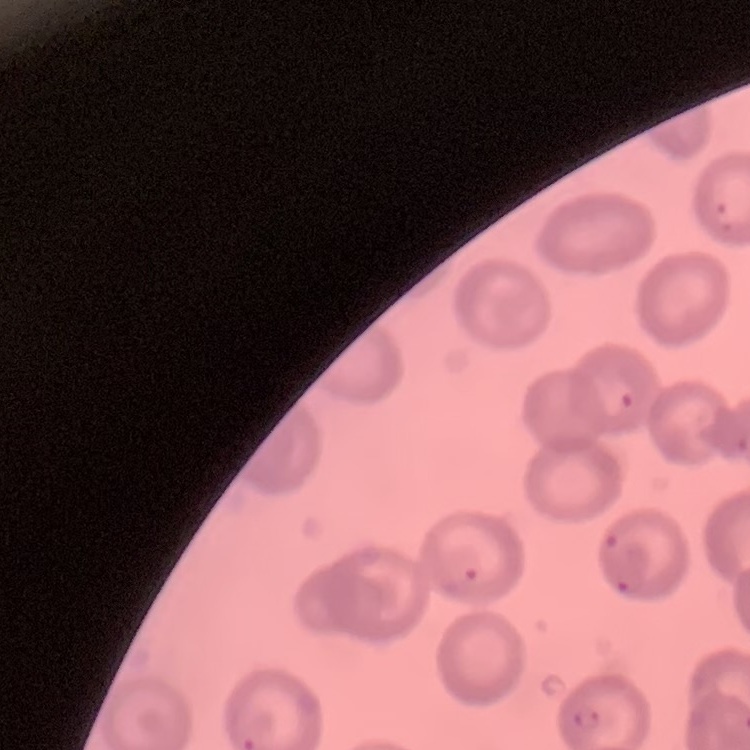
Summary:
  - Erythrocyte morphology: no rouleaux formation
  - Image type: one tile cut from a larger photomicrograph
  - Stain: Field's or Giemsa
  - Preparation: thin peripheral smear